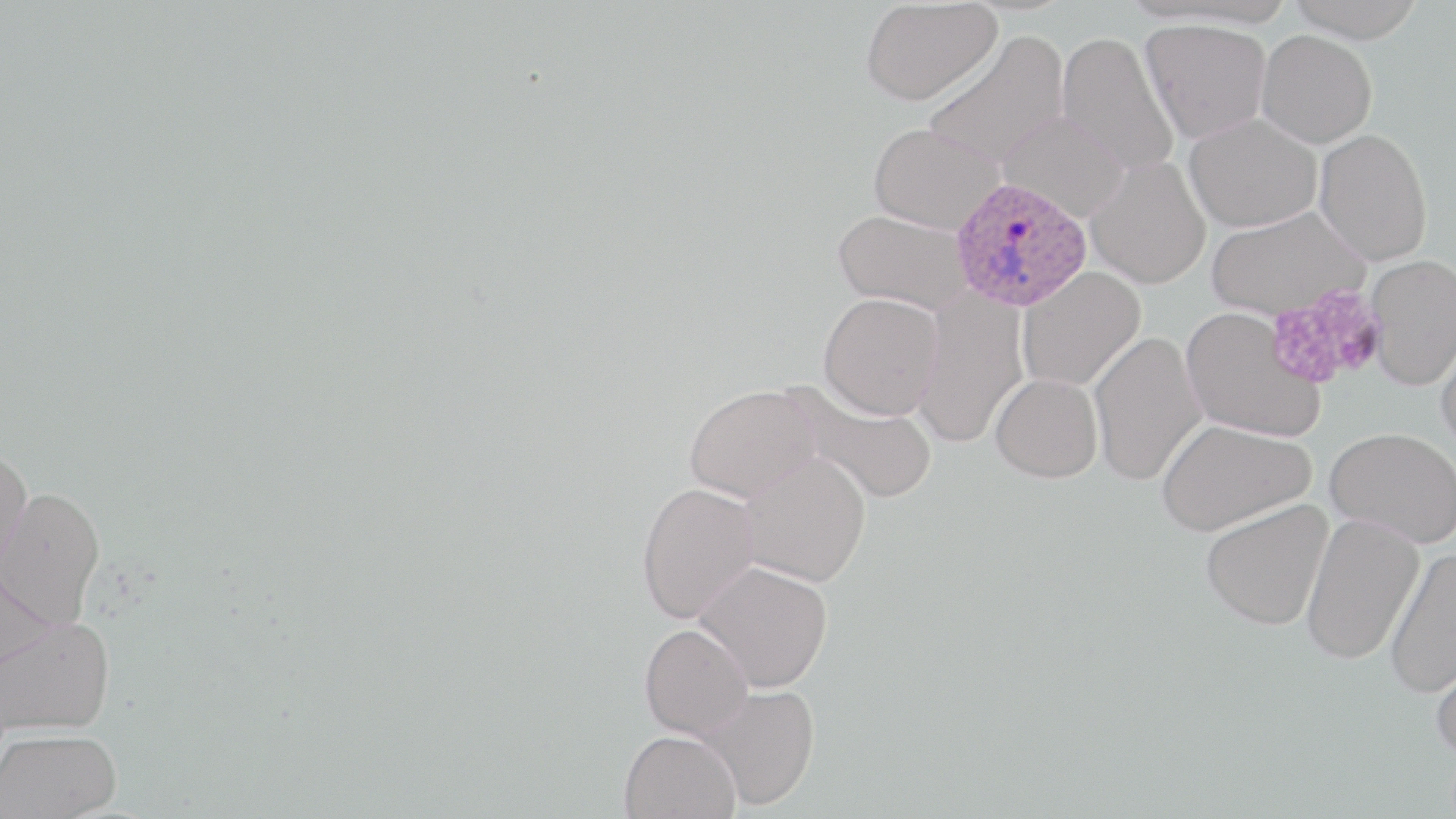
Summary:
  - Coordinate format: approximate bounding boxes as named x1/y1/x2/y2 corners in pixels
  - Uninfected red blood cell locations: (x1=1285, y1=0, x2=1426, y2=43), (x1=861, y1=1, x2=1001, y2=105), (x1=1140, y1=18, x2=1272, y2=143), (x1=923, y1=30, x2=1071, y2=170), (x1=1056, y1=30, x2=1179, y2=176), (x1=1255, y1=30, x2=1377, y2=148), (x1=997, y1=110, x2=1130, y2=221), (x1=1184, y1=113, x2=1322, y2=233), (x1=867, y1=123, x2=1003, y2=233), (x1=1314, y1=129, x2=1432, y2=266), (x1=1085, y1=156, x2=1211, y2=289), (x1=1206, y1=206, x2=1370, y2=320), (x1=834, y1=208, x2=974, y2=316), (x1=1365, y1=254, x2=1456, y2=390), (x1=1017, y1=266, x2=1146, y2=392), (x1=913, y1=291, x2=1028, y2=447), (x1=818, y1=292, x2=943, y2=420), (x1=1180, y1=307, x2=1326, y2=443), (x1=1435, y1=329, x2=1456, y2=455), (x1=1089, y1=331, x2=1207, y2=485), (x1=990, y1=373, x2=1103, y2=482), (x1=783, y1=380, x2=939, y2=504), (x1=684, y1=384, x2=823, y2=502), (x1=1156, y1=418, x2=1314, y2=536), (x1=1324, y1=427, x2=1456, y2=548), (x1=0, y1=446, x2=34, y2=582), (x1=738, y1=452, x2=871, y2=587), (x1=636, y1=482, x2=761, y2=624), (x1=0, y1=485, x2=106, y2=628), (x1=1201, y1=499, x2=1333, y2=630), (x1=1300, y1=513, x2=1425, y2=664), (x1=1385, y1=546, x2=1456, y2=698), (x1=0, y1=559, x2=54, y2=674), (x1=694, y1=560, x2=833, y2=691), (x1=1, y1=616, x2=117, y2=736), (x1=639, y1=623, x2=753, y2=739), (x1=1429, y1=641, x2=1456, y2=760), (x1=698, y1=684, x2=820, y2=810), (x1=1, y1=728, x2=122, y2=819), (x1=619, y1=729, x2=740, y2=819)
  - Platelet locations: (x1=1266, y1=285, x2=1386, y2=392)
  - Plasmodium ovale-infected red blood cell locations: (x1=950, y1=175, x2=1092, y2=312)
  - Slide-level diagnosis: Plasmodium ovale
  - Field of view: one of a larger specimen
  - Modality: light microscopy
  - Image size: 1456×819 pixels
  - Magnification: 1000x
  - Preparation: thin blood film
  - Stain: May-Grünwald-Giemsa